Outline each blood parasite and name the species.
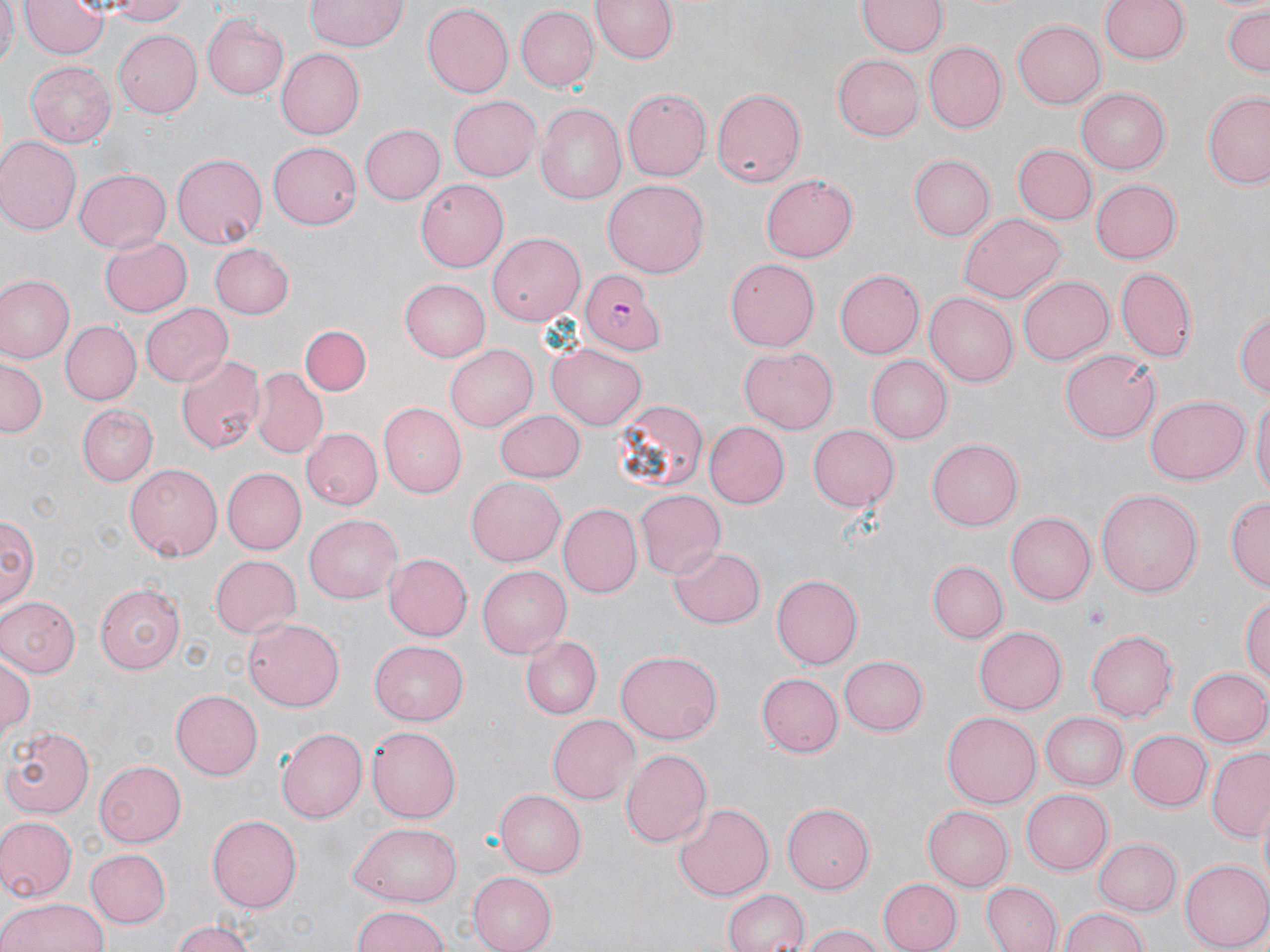
Approximate bounding boxes as [x1, y1, x2, y2] in pixels.
Plasmodium falciparum-infected red blood cells: [581, 271, 661, 351].
No Plasmodium ovale, Plasmodium malariae, Plasmodium vivax, Babesia divergens, or Trypanosoma brucei observed.

Uninfected red blood cell locations: [0, 0, 18, 72], [21, 0, 109, 58], [106, 0, 194, 25], [305, 0, 406, 53], [588, 0, 681, 66], [859, 0, 946, 57], [1098, 0, 1191, 65], [420, 4, 512, 98], [513, 5, 599, 93], [1221, 6, 1270, 77], [202, 13, 288, 100], [1013, 20, 1105, 109], [112, 27, 201, 119], [922, 40, 1006, 135], [277, 49, 364, 138], [834, 55, 923, 141], [25, 60, 116, 149], [624, 87, 713, 181], [711, 88, 806, 189], [1077, 89, 1169, 174], [1203, 91, 1270, 189], [448, 95, 541, 181], [533, 105, 625, 206], [360, 124, 447, 204], [0, 138, 79, 235], [267, 142, 360, 229], [1012, 145, 1096, 225], [172, 153, 269, 249], [911, 154, 996, 240], [74, 168, 171, 253], [761, 174, 860, 263], [1090, 176, 1180, 261], [414, 179, 509, 273], [602, 180, 709, 278], [960, 212, 1065, 303], [488, 232, 584, 324], [100, 233, 192, 317], [210, 243, 295, 319], [724, 258, 820, 352], [1117, 266, 1196, 360], [834, 269, 924, 359], [1018, 274, 1114, 363], [2, 276, 73, 361], [400, 276, 493, 362], [926, 293, 1016, 388], [139, 303, 231, 388], [1234, 305, 1270, 402], [60, 321, 140, 404], [301, 324, 370, 396], [548, 343, 646, 429], [446, 344, 541, 432], [739, 348, 838, 432], [1060, 349, 1161, 443], [176, 354, 266, 455], [0, 356, 47, 436], [867, 357, 952, 444], [253, 370, 328, 458], [1249, 394, 1269, 503], [1145, 395, 1249, 483], [612, 398, 709, 497], [377, 404, 466, 498], [77, 405, 159, 485], [495, 409, 586, 484], [706, 422, 788, 509], [806, 424, 899, 511], [301, 427, 383, 510], [928, 439, 1023, 530], [125, 461, 225, 559], [220, 467, 303, 554], [466, 474, 565, 564], [1096, 488, 1204, 599], [634, 489, 725, 579], [1225, 495, 1270, 590], [558, 503, 642, 599], [2, 513, 37, 613], [1006, 513, 1095, 605], [304, 514, 402, 603], [671, 546, 765, 630], [383, 552, 472, 641], [208, 554, 300, 639], [928, 560, 1008, 643], [476, 565, 570, 658], [772, 574, 861, 666], [94, 583, 185, 672], [1242, 593, 1270, 689], [0, 596, 79, 677], [244, 617, 345, 710], [975, 626, 1067, 715], [1087, 629, 1176, 722], [519, 635, 603, 720], [370, 641, 468, 725], [1, 650, 36, 740], [614, 650, 723, 744], [838, 653, 927, 734], [1186, 667, 1270, 748], [756, 673, 842, 757], [171, 691, 263, 779], [943, 712, 1040, 808], [1041, 712, 1128, 789], [548, 713, 640, 804], [4, 725, 96, 816], [277, 725, 367, 824], [367, 725, 462, 822], [1124, 729, 1212, 811], [620, 747, 712, 847], [1205, 749, 1270, 842], [94, 760, 186, 845], [496, 788, 589, 877], [1022, 789, 1113, 875], [673, 802, 772, 903], [784, 803, 878, 894], [924, 804, 1013, 891], [209, 814, 305, 912], [0, 817, 76, 900], [346, 823, 462, 906], [1093, 838, 1182, 914], [86, 849, 170, 929], [1182, 860, 1270, 951], [468, 872, 556, 952], [879, 877, 961, 952], [982, 881, 1062, 952], [723, 889, 809, 952], [0, 896, 108, 952], [351, 905, 449, 952], [1062, 908, 1149, 952], [170, 920, 259, 952], [799, 924, 882, 952]. Slide-level diagnosis: Plasmodium falciparum. May-Grünwald-Giemsa-stained preparation. Light microscopy. Image is 1270×952 pixels. Captured at 1000x magnification. Single field of view. Thin blood film.